Name the parasite shown.
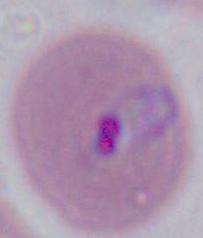

This is Plasmodium.

{
  "modality": "photomicrograph",
  "magnification": "400x or 1000x"
}